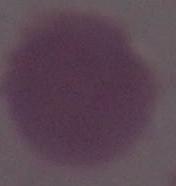
Photomicrograph. A red blood cell is shown. 1000x magnification.